Describe the morphology of the erythrocytes.
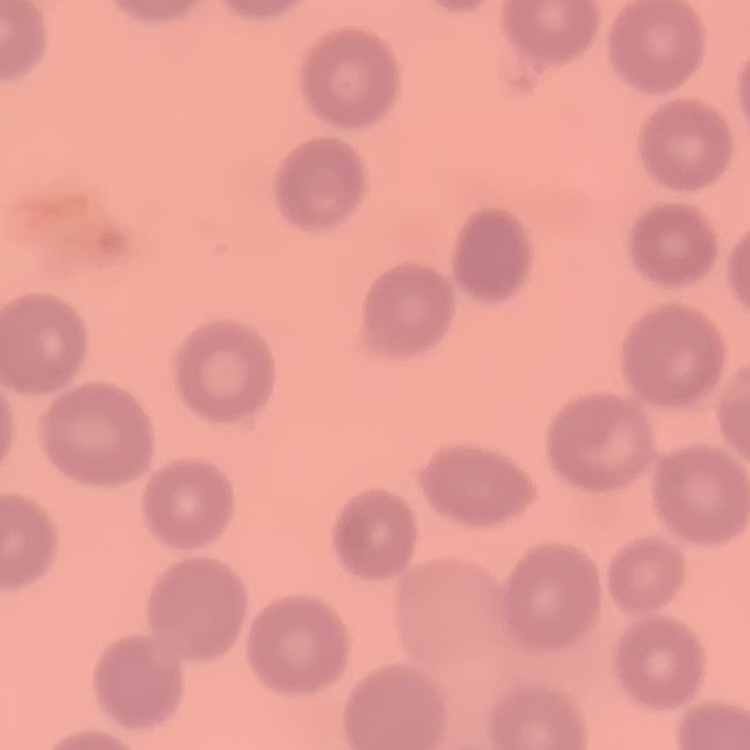
No rouleaux formation.

preparation: thin peripheral smear
stain: Field's or Giemsa
image_type: square crop of a larger photomicrograph